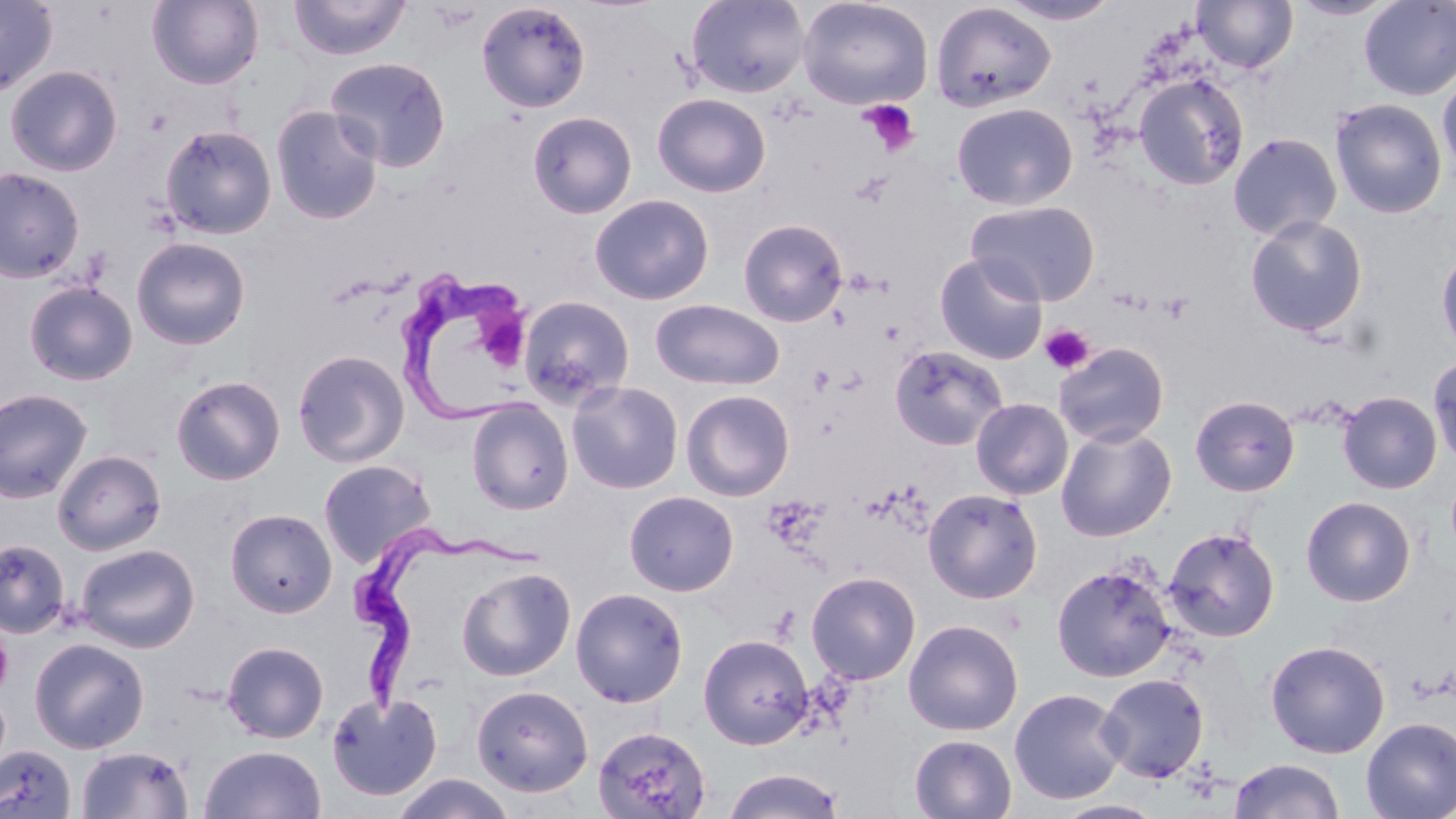
Summary:
  - Coordinate format: approximate bounding boxes as (x1,y1)-(x2,y2) corner pairs in pixels
  - Platelet locations: (860,100)-(921,157), (851,171)-(894,208), (1158,293)-(1194,323), (1040,324)-(1094,374), (0,623)-(13,698)
  - Uninfected red blood cell locations: (0,0)-(58,98), (147,0)-(263,89), (289,0)-(410,61), (686,0)-(809,98), (797,0)-(933,111), (995,0)-(1123,26), (1192,0)-(1297,73), (1289,0)-(1399,21), (1358,0)-(1456,100), (476,1)-(592,113), (930,1)-(1057,113), (325,56)-(452,172), (4,64)-(123,176), (1437,69)-(1456,183), (1133,73)-(1248,191), (652,92)-(771,198), (1330,98)-(1447,219), (951,102)-(1078,210), (270,105)-(384,225), (527,111)-(637,219), (159,124)-(277,239), (1227,132)-(1343,241), (0,166)-(85,283), (589,194)-(715,305), (965,199)-(1101,307), (1244,215)-(1368,337), (738,218)-(848,327), (131,237)-(251,350), (1436,244)-(1456,359), (934,252)-(1049,365), (23,281)-(138,385), (518,295)-(636,408), (650,299)-(785,391), (1053,342)-(1170,447), (889,344)-(1009,451), (292,348)-(411,468), (1428,353)-(1456,468), (171,374)-(286,485), (566,380)-(684,494), (0,388)-(94,503), (681,389)-(795,501), (1337,391)-(1443,494), (1190,394)-(1301,496), (971,398)-(1074,500), (466,399)-(573,514), (1055,424)-(1177,542), (52,450)-(166,555), (318,459)-(436,569), (923,487)-(1044,603), (624,490)-(739,596), (1300,496)-(1417,607), (225,508)-(338,617), (1163,526)-(1280,642), (0,538)-(70,639), (76,543)-(201,653), (1051,562)-(1177,682), (456,566)-(576,682), (806,571)-(921,685), (570,587)-(689,707), (903,618)-(1024,736), (698,633)-(815,749), (29,637)-(150,753), (1265,639)-(1391,758), (222,640)-(329,743), (1096,673)-(1210,783), (471,684)-(593,797), (1009,687)-(1128,805), (325,691)-(444,801), (1360,716)-(1456,819), (591,725)-(712,819), (909,734)-(1017,818), (0,744)-(77,818), (199,744)-(326,818), (76,745)-(195,818), (1229,758)-(1346,819), (720,768)-(846,818), (390,773)-(516,819), (1052,800)-(1166,819)
  - Trypanosoma brucei locations: (398,268)-(540,424), (340,521)-(563,721)
  - Slide-level diagnosis: Trypanosoma brucei
  - Preparation: thin blood smear
  - Modality: light microscopy
  - Stain: May-Grünwald-Giemsa
  - Field of view: single
  - Image size: 1456×819 pixels
  - Magnification: 1000x